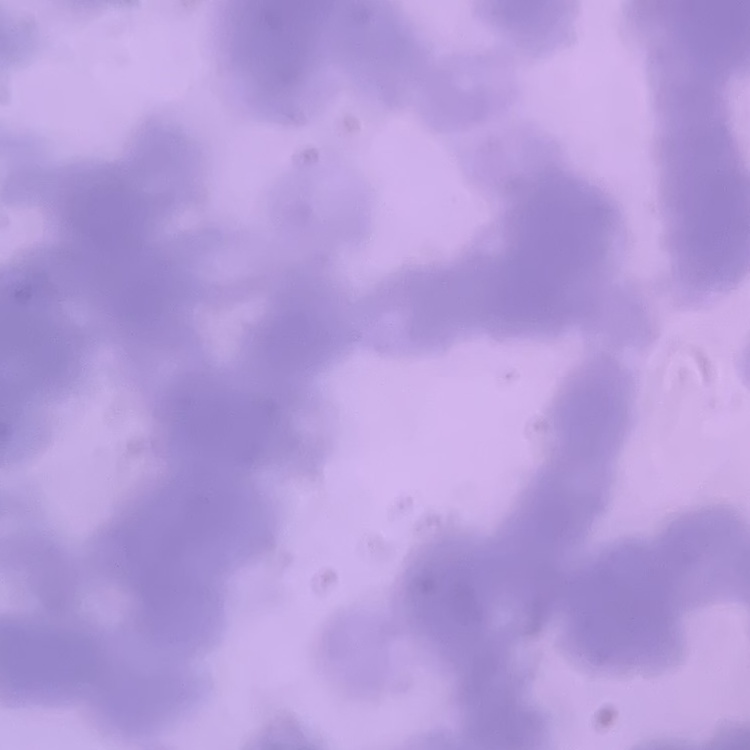
{
  "red_blood_cell_morphology": "rouleaux formation",
  "preparation": "thin peripheral smear",
  "image_type": "one tile cut from a larger photomicrograph",
  "stain": "Field's or Giemsa"
}